Locate and identify every blood parasite.
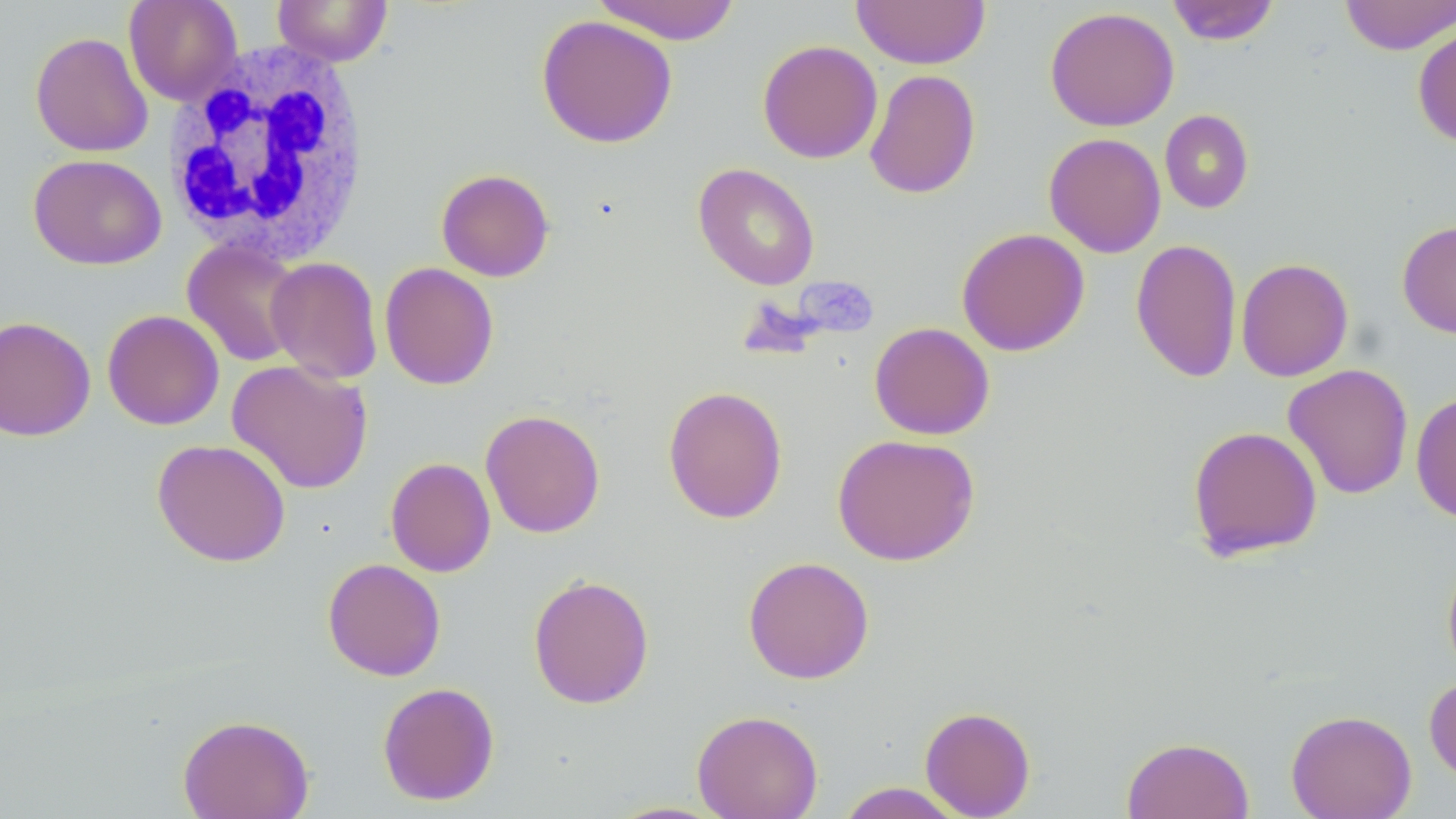

No blood parasites observed.

slide-level diagnosis = negative for blood parasites
magnification = 1000x
field of view = one of a larger specimen
image size = 1456×819 pixels
stain = May-Grünwald-Giemsa
white blood cell locations = approximate bounding boxes as (x1,y1)-(x2,y2) corner pairs in pixels: (164,42)-(373,266)
uninfected red blood cell locations = approximate bounding boxes as (x1,y1)-(x2,y2) corner pairs in pixels: (124,0)-(243,105), (272,0)-(393,66), (591,0)-(742,44), (852,0)-(991,69), (1339,0)-(1455,55), (1166,1)-(1281,45), (1044,6)-(1179,132), (536,14)-(678,148), (1413,23)-(1456,148), (29,31)-(153,158), (757,40)-(882,164), (864,68)-(981,200), (1159,109)-(1254,213), (1043,132)-(1166,258), (28,153)-(166,270), (693,162)-(820,290), (436,168)-(555,281), (1397,219)-(1456,339), (956,227)-(1090,356), (1131,238)-(1243,383), (182,239)-(305,367), (265,257)-(383,384), (1235,257)-(1354,382), (379,262)-(499,390), (102,309)-(224,430), (0,315)-(96,441), (869,321)-(995,440), (226,359)-(374,495), (1282,363)-(1414,500), (662,385)-(788,524), (1411,391)-(1456,524), (480,408)-(605,538), (1186,425)-(1323,562), (832,433)-(980,566), (152,438)-(291,567), (385,457)-(496,577), (1442,552)-(1456,679), (743,555)-(874,684), (322,558)-(446,681), (528,573)-(655,709), (1424,675)-(1456,787), (377,681)-(500,806), (919,706)-(1036,818), (692,709)-(824,819), (1285,709)-(1417,819), (177,714)-(314,818), (1121,736)-(1254,819), (835,782)-(966,818), (601,800)-(734,819)
modality = optical microscopy
preparation = thin blood film